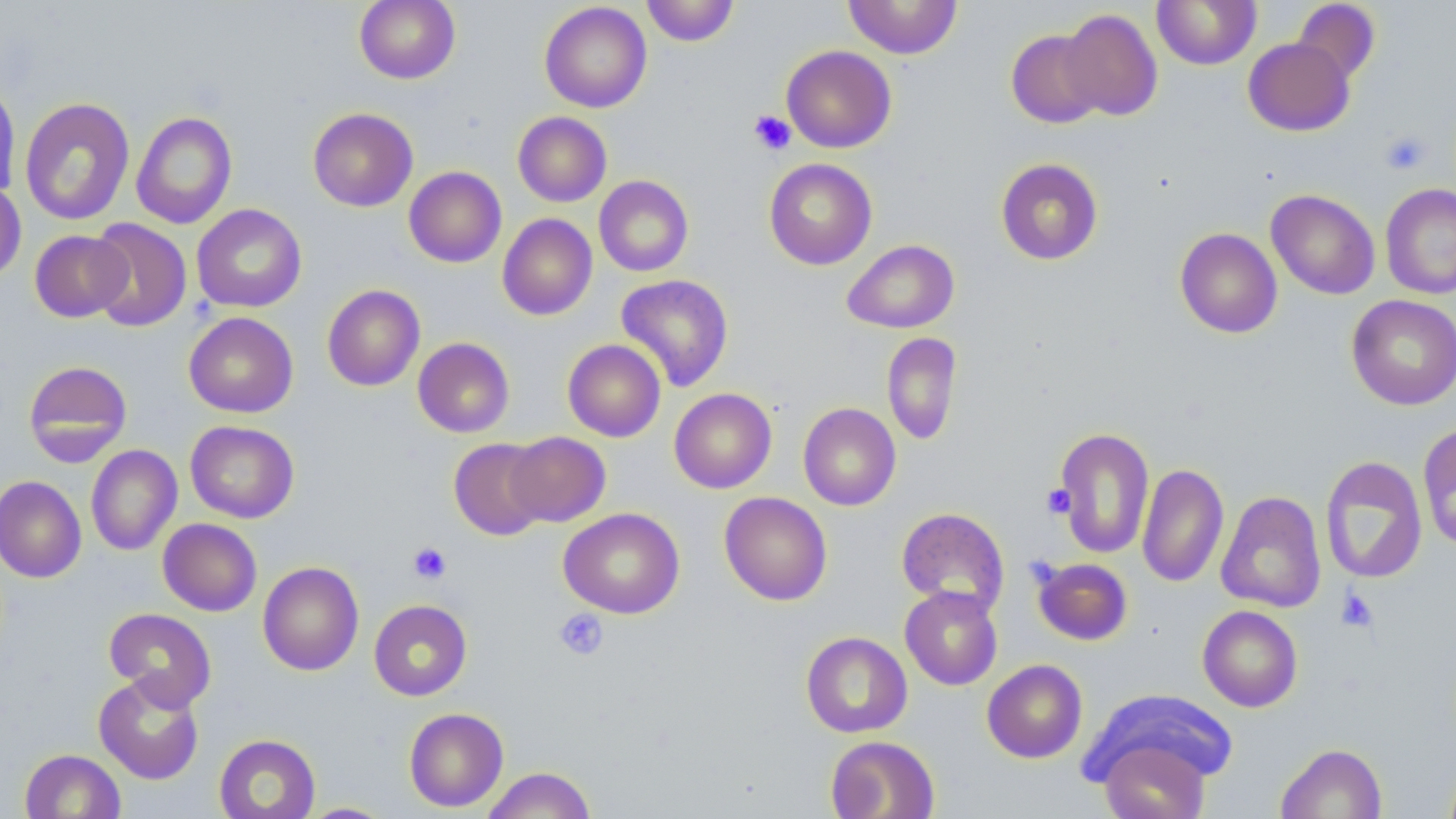

slide-level diagnosis = negative for blood parasites
stain = May-Grünwald-Giemsa
magnification = 1000x
field of view = single
image size = 1456×819 pixels
preparation = thin blood smear
platelet locations = approximate bounding boxes as (x1,y1)-(x2,y2) corner pairs in pixels: (749,109)-(797,156), (1379,130)-(1431,176), (1042,484)-(1076,519), (408,542)-(452,584), (1336,587)-(1379,632), (554,609)-(609,661)
modality = light microscopy
uninfected red blood cell locations = approximate bounding boxes as (x1,y1)-(x2,y2) corner pairs in pixels: (354,0)-(460,84), (641,0)-(740,46), (843,0)-(963,59), (1152,0)-(1262,70), (1292,1)-(1381,84), (539,2)-(652,113), (1058,9)-(1163,121), (1005,29)-(1106,128), (1243,37)-(1354,136), (781,45)-(896,152), (0,79)-(22,199), (20,97)-(135,225), (307,107)-(418,212), (131,111)-(237,229), (513,111)-(611,207), (764,158)-(877,270), (995,158)-(1104,265), (404,166)-(506,267), (594,176)-(694,276), (0,181)-(26,284), (1380,182)-(1456,300), (1266,189)-(1380,300), (191,204)-(307,312), (497,214)-(597,320), (87,219)-(192,332), (1175,228)-(1283,338), (30,230)-(132,322), (842,239)-(959,334), (616,273)-(734,392), (322,284)-(425,391), (1346,294)-(1456,410), (184,312)-(298,417), (882,332)-(962,445), (413,337)-(514,437), (562,339)-(666,442), (23,360)-(132,466), (669,388)-(777,493), (798,403)-(901,510), (185,420)-(299,523), (1417,421)-(1456,552), (1052,427)-(1155,560), (504,431)-(611,527), (448,438)-(551,540), (85,445)-(182,556), (1319,456)-(1428,584), (1137,463)-(1229,588), (1135,473)-(1327,591), (0,476)-(86,583), (719,491)-(832,606), (1216,491)-(1327,613), (559,507)-(685,618), (897,507)-(1010,613), (158,518)-(262,616), (1033,558)-(1133,646), (258,561)-(364,676), (900,586)-(1003,690), (368,599)-(472,701), (1197,605)-(1303,712), (103,608)-(217,710), (801,631)-(912,738), (982,660)-(1087,763), (93,673)-(205,784), (1089,690)-(1237,790), (404,707)-(508,812), (214,733)-(321,819), (825,735)-(940,818), (1098,735)-(1211,819), (1275,743)-(1387,819), (19,749)-(126,818), (481,767)-(596,819), (297,803)-(396,818)